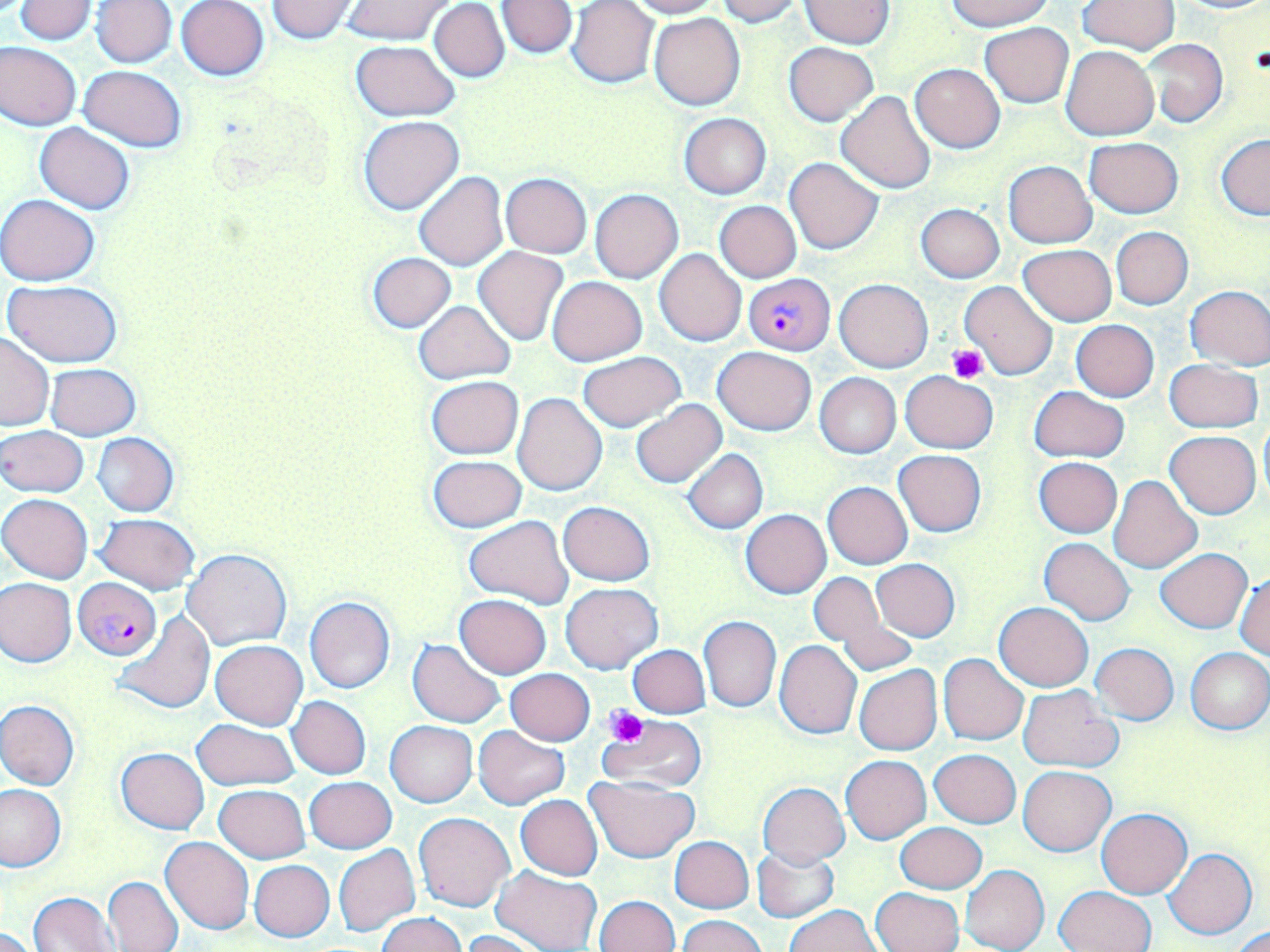 Approximate bounding boxes as (x1, y1, x2, y2) in pixels. Uninfected red blood cell locations: (13, 0, 96, 43), (343, 0, 454, 45), (625, 0, 720, 18), (715, 0, 802, 25), (800, 0, 892, 48), (948, 0, 1053, 31), (1172, 0, 1270, 14), (90, 1, 177, 67), (177, 1, 270, 80), (265, 1, 360, 42), (496, 1, 577, 58), (567, 1, 659, 88), (1077, 1, 1178, 53), (429, 2, 509, 82), (648, 13, 745, 110), (981, 22, 1072, 106), (1140, 39, 1227, 127), (350, 40, 460, 121), (0, 42, 82, 130), (783, 42, 877, 125), (1060, 44, 1160, 140), (910, 63, 1005, 152), (78, 65, 187, 151), (837, 91, 936, 194), (679, 113, 771, 198), (358, 115, 464, 215), (35, 123, 134, 214), (1217, 135, 1270, 220), (1084, 136, 1184, 219), (784, 157, 883, 254), (1004, 160, 1096, 247), (414, 172, 508, 270), (500, 173, 591, 257), (591, 189, 683, 283), (0, 194, 99, 286), (714, 200, 801, 282), (917, 203, 1004, 282), (1111, 227, 1193, 310), (1018, 245, 1116, 325), (473, 247, 568, 346), (656, 249, 747, 345), (366, 252, 456, 333), (547, 275, 647, 366), (835, 278, 933, 372), (960, 279, 1059, 379), (4, 280, 125, 367), (1186, 285, 1270, 370), (413, 300, 516, 384), (1071, 319, 1159, 401), (0, 333, 54, 431), (713, 346, 816, 436), (577, 352, 687, 432), (1164, 359, 1262, 432), (45, 363, 140, 440), (900, 371, 998, 453), (815, 373, 902, 458), (425, 375, 524, 459), (1030, 386, 1128, 463), (514, 393, 606, 496), (631, 401, 726, 488), (1258, 421, 1270, 503), (1, 425, 89, 498), (1164, 430, 1262, 518), (91, 432, 179, 516), (683, 449, 768, 533), (894, 450, 986, 536), (429, 455, 525, 532), (1034, 457, 1122, 537), (1107, 474, 1202, 573), (823, 482, 912, 569), (1, 495, 93, 583), (559, 501, 655, 586), (740, 509, 832, 598), (94, 513, 199, 594), (464, 516, 571, 608), (1039, 537, 1135, 626), (1155, 548, 1251, 633), (182, 549, 291, 651), (871, 560, 960, 641), (808, 571, 892, 652), (1234, 571, 1270, 660), (0, 578, 76, 667), (562, 582, 661, 673), (455, 594, 552, 678), (305, 597, 395, 694), (994, 602, 1094, 691), (834, 608, 917, 675), (112, 611, 214, 715), (699, 616, 781, 712), (408, 639, 505, 727), (211, 640, 307, 729), (774, 640, 861, 739), (1091, 642, 1178, 724), (628, 645, 709, 718), (1185, 648, 1269, 734), (939, 654, 1029, 746), (854, 666, 943, 755), (505, 668, 594, 744), (1017, 686, 1122, 772), (287, 696, 371, 779), (0, 700, 79, 791), (599, 715, 708, 791), (192, 718, 300, 791), (386, 721, 477, 806), (472, 725, 570, 809), (115, 747, 209, 833), (930, 750, 1020, 827), (841, 755, 931, 843), (1019, 766, 1114, 855), (585, 775, 700, 862), (305, 776, 396, 854), (0, 782, 65, 872), (757, 783, 849, 867), (213, 784, 311, 862), (515, 795, 603, 880), (1097, 808, 1193, 898), (414, 812, 515, 911), (896, 822, 986, 893), (160, 836, 254, 934), (671, 836, 753, 913), (334, 846, 421, 937), (752, 847, 839, 922), (1163, 848, 1256, 938), (249, 860, 334, 941), (960, 864, 1049, 952), (491, 866, 602, 952), (103, 876, 184, 952), (1054, 885, 1156, 952), (870, 887, 963, 952), (29, 892, 119, 952), (595, 895, 680, 952), (785, 905, 880, 952), (376, 913, 468, 952), (677, 914, 768, 952), (1229, 925, 1270, 951), (0, 926, 41, 952), (461, 930, 544, 952). Platelet locations: (949, 344, 988, 382), (605, 705, 648, 747). Plasmodium falciparum-infected red blood cell locations: (743, 273, 834, 354), (74, 578, 160, 659). Slide-level diagnosis: Plasmodium falciparum. Light microscopy. May-Grünwald-Giemsa-stained preparation. One field of a larger specimen. Thin blood film. Captured at 1000x magnification. Image is 1270×952 pixels.